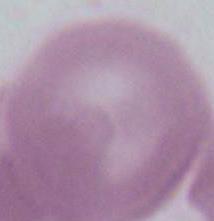

Summary:
  - Modality: photomicrograph
  - Identification: erythrocyte
  - Magnification: 1000x